Name the parasite shown.
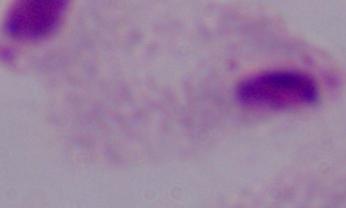
This is a trichomonad.

modality = micrograph
magnification = 1000x